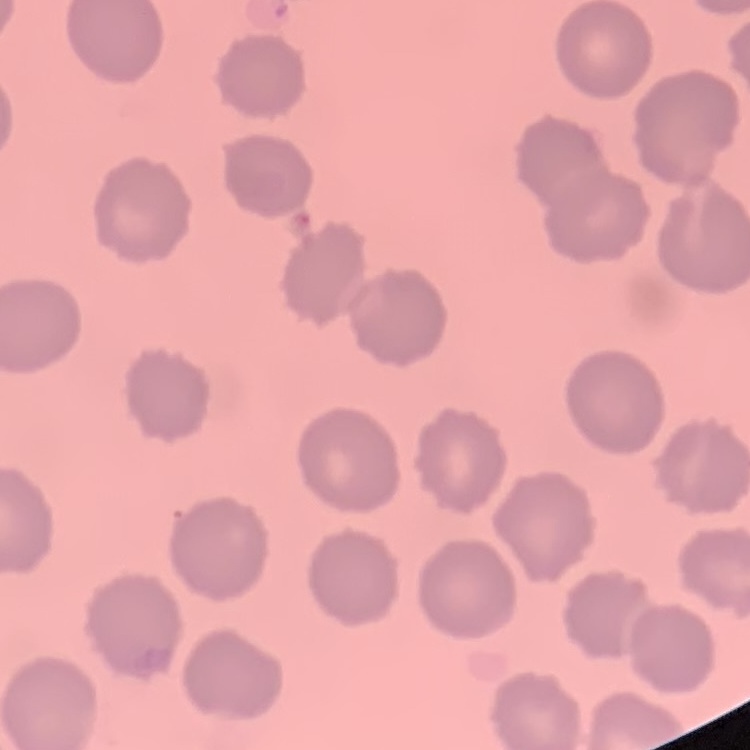

The red blood cells exhibit no rouleaux formation. Stained with either Field's or Giemsa. One tile cut from a larger photomicrograph. Thin blood smear.